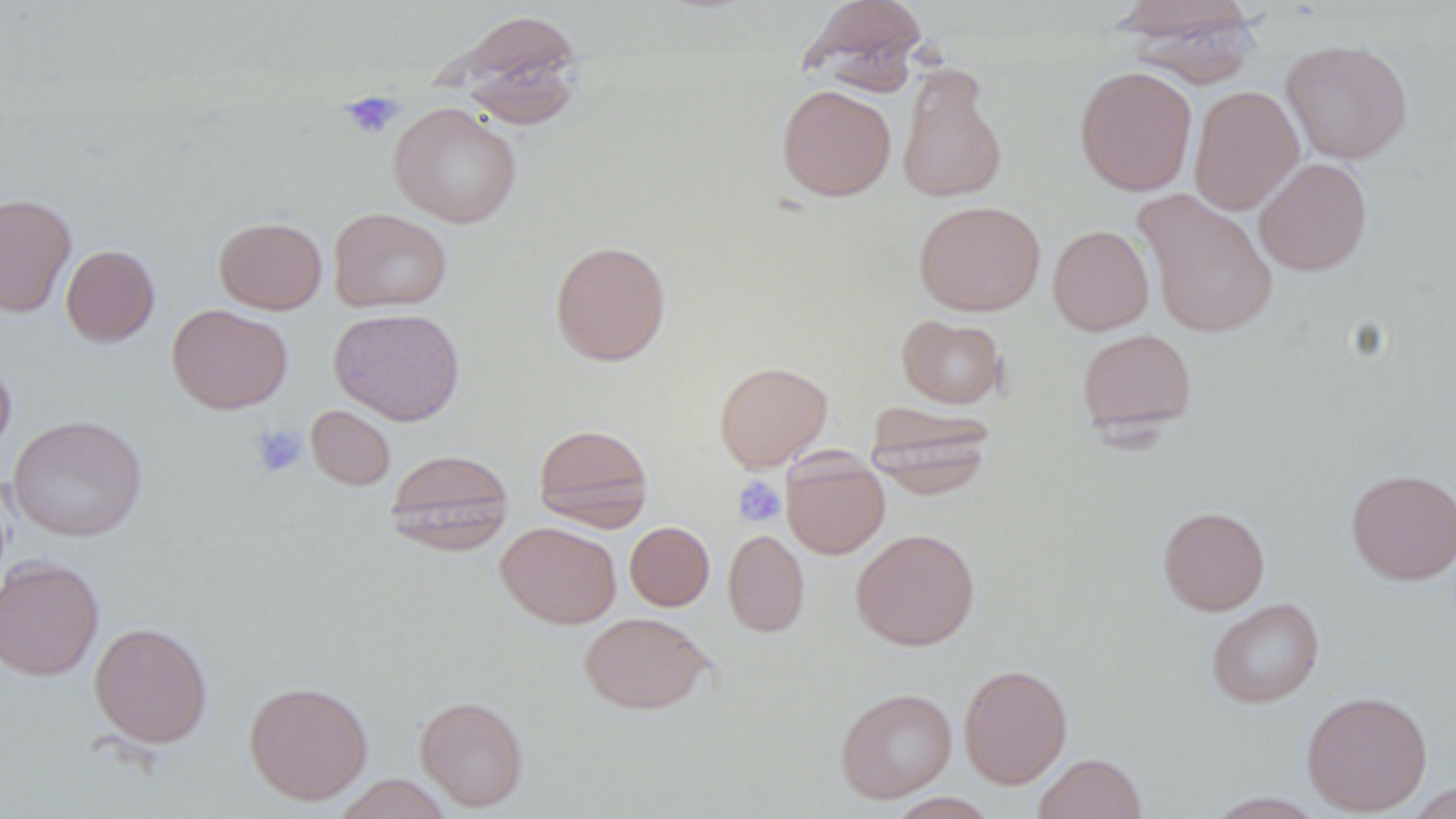

Summary:
  - Coordinate format: approximate bounding boxes as [x1, y1, x2, y2] in pixels
  - Platelet locations: [340, 90, 404, 140], [248, 424, 308, 477], [732, 476, 786, 527]
  - Uninfected red blood cell locations: [801, 0, 928, 92], [1113, 0, 1261, 85], [445, 9, 585, 126], [1281, 40, 1412, 164], [896, 64, 1007, 205], [1074, 65, 1197, 196], [776, 84, 896, 201], [1188, 85, 1304, 215], [388, 102, 522, 228], [1254, 158, 1372, 275], [1134, 190, 1278, 338], [0, 193, 76, 317], [914, 200, 1046, 316], [328, 207, 452, 313], [214, 217, 327, 314], [1048, 225, 1154, 335], [550, 240, 671, 365], [61, 244, 159, 346], [167, 304, 292, 414], [329, 307, 465, 426], [897, 314, 1007, 408], [1076, 328, 1196, 435], [0, 354, 15, 460], [714, 361, 832, 471], [866, 402, 996, 497], [306, 405, 395, 490], [8, 415, 147, 541], [533, 422, 653, 531], [384, 448, 514, 553], [781, 451, 890, 559], [1346, 468, 1456, 584], [1158, 506, 1269, 615], [624, 521, 714, 611], [496, 522, 621, 629], [723, 529, 809, 637], [851, 529, 980, 650], [0, 556, 103, 681], [1207, 598, 1324, 708], [580, 612, 711, 714], [89, 622, 213, 747], [959, 663, 1072, 788], [244, 680, 373, 804], [835, 687, 957, 802], [1302, 691, 1433, 815], [415, 695, 529, 811], [1034, 753, 1147, 819], [333, 774, 454, 818], [1404, 781, 1456, 817], [886, 792, 1000, 818], [1201, 792, 1328, 818]
  - Slide-level diagnosis: negative for blood parasites
  - Modality: light microscopy
  - Field of view: single
  - Preparation: thin blood film
  - Image size: 1456×819 pixels
  - Magnification: 1000x
  - Stain: May-Grünwald-Giemsa